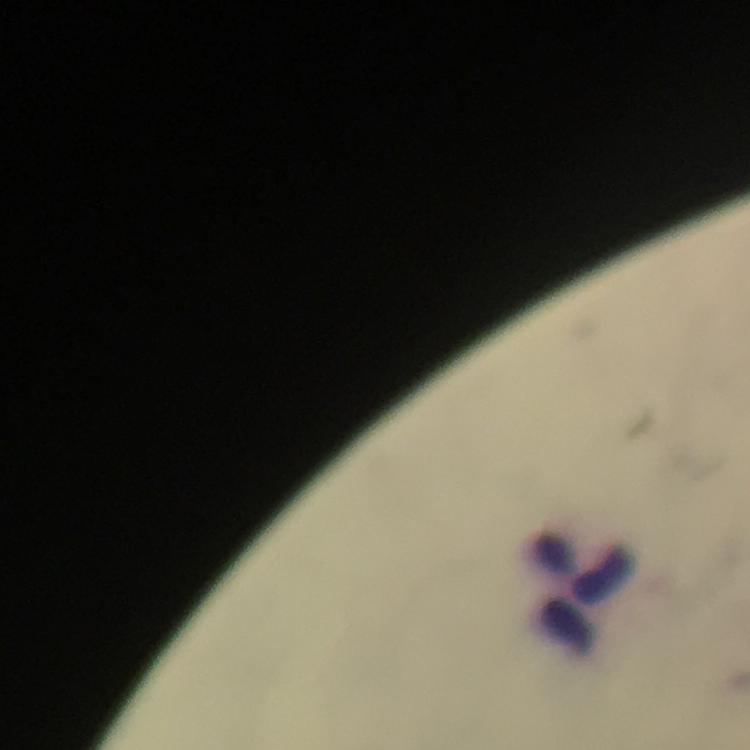
Approximate centers as (x, y) in pixels. Leukocyte locations: (584, 592). Giemsa-stained preparation. Thick blood smear. Malaria parasites: none seen. 100x magnification. Photographed through the microscope with a smartphone camera. Cropped region of a single field of view. Immersion oil applied. From a malaria diagnostic workup. Image is 750×750 pixels.